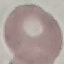

Result: no malaria parasites detected. Giemsa-stained preparation. Automatically extracted cell patch, resized to 64 × 64 pixels. Photographed with a smartphone camera at the microscope eyepiece. Thin smear of blood.